Outline each Plasmodium vivax-infected red blood cell.
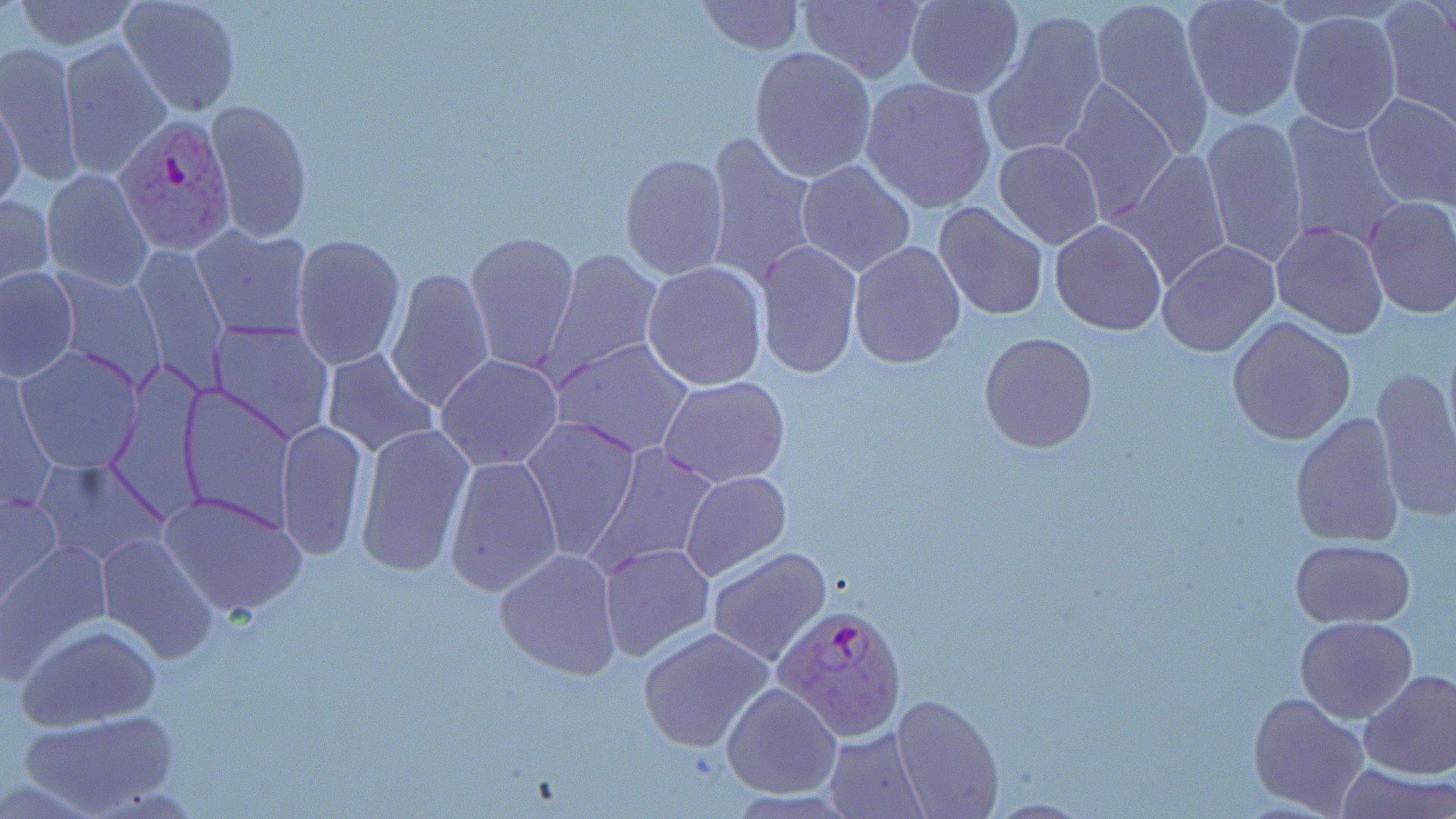

Approximate bounding boxes as (x1, y1, x2, y2) in pixels.
Plasmodium vivax-infected red blood cells: (112, 111, 237, 255), (775, 605, 907, 740).

Uninfected red blood cell locations: (10, 0, 144, 51), (119, 0, 243, 117), (693, 0, 806, 54), (796, 0, 927, 84), (903, 0, 1024, 98), (1091, 0, 1217, 159), (1178, 2, 1305, 122), (1378, 2, 1456, 127), (980, 9, 1109, 160), (1286, 10, 1402, 135), (1010, 29, 1167, 197), (58, 37, 174, 179), (0, 41, 83, 187), (748, 45, 877, 182), (860, 77, 998, 214), (1057, 78, 1180, 224), (1360, 92, 1456, 209), (0, 98, 26, 212), (205, 98, 313, 242), (1278, 113, 1408, 253), (1201, 115, 1309, 267), (700, 130, 821, 291), (993, 139, 1104, 249), (1115, 147, 1233, 289), (619, 152, 732, 281), (797, 160, 918, 276), (41, 169, 154, 290), (0, 192, 54, 293), (1362, 194, 1456, 319), (933, 200, 1050, 320), (1049, 220, 1168, 335), (1270, 221, 1389, 339), (189, 224, 313, 344), (462, 231, 580, 375), (291, 233, 405, 370), (754, 240, 863, 378), (847, 240, 966, 370), (1156, 240, 1281, 357), (130, 243, 231, 392), (541, 247, 663, 383), (642, 261, 767, 391), (0, 265, 80, 380), (385, 265, 496, 413), (47, 268, 166, 387), (1227, 315, 1357, 445), (207, 321, 335, 447), (978, 332, 1099, 454), (551, 337, 698, 458), (16, 345, 144, 473), (320, 349, 439, 460), (437, 354, 564, 472), (1372, 364, 1456, 523), (1, 366, 56, 512), (658, 376, 791, 487), (175, 384, 295, 532), (1289, 411, 1405, 548), (519, 415, 642, 562), (276, 419, 369, 561), (354, 423, 475, 579), (584, 442, 721, 576), (31, 455, 169, 568), (443, 455, 562, 596), (680, 470, 792, 581), (0, 491, 61, 604), (160, 492, 306, 617), (95, 532, 218, 662), (1290, 537, 1416, 628), (1, 541, 109, 677), (598, 542, 716, 663), (706, 546, 833, 666), (494, 549, 623, 680), (1295, 617, 1417, 722), (19, 624, 161, 731), (639, 628, 774, 753), (1359, 670, 1456, 780), (722, 682, 843, 799), (1247, 691, 1371, 818), (889, 694, 1006, 818), (19, 711, 177, 818), (825, 727, 931, 819), (1338, 764, 1453, 819). Slide-level diagnosis: Plasmodium vivax. Thin blood film. Image is 1456×819 pixels. Single field of view. May-Grünwald-Giemsa-stained preparation. Captured at 1000x magnification. Optical microscopy.